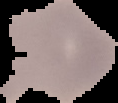
Image is 118×103 pixels. The area outside the segmented cell region is set to black. From a thin blood film. Malaria status: uninfected.